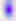

modality: photomicrograph
identification: Toxoplasma gondii
magnification: 400x